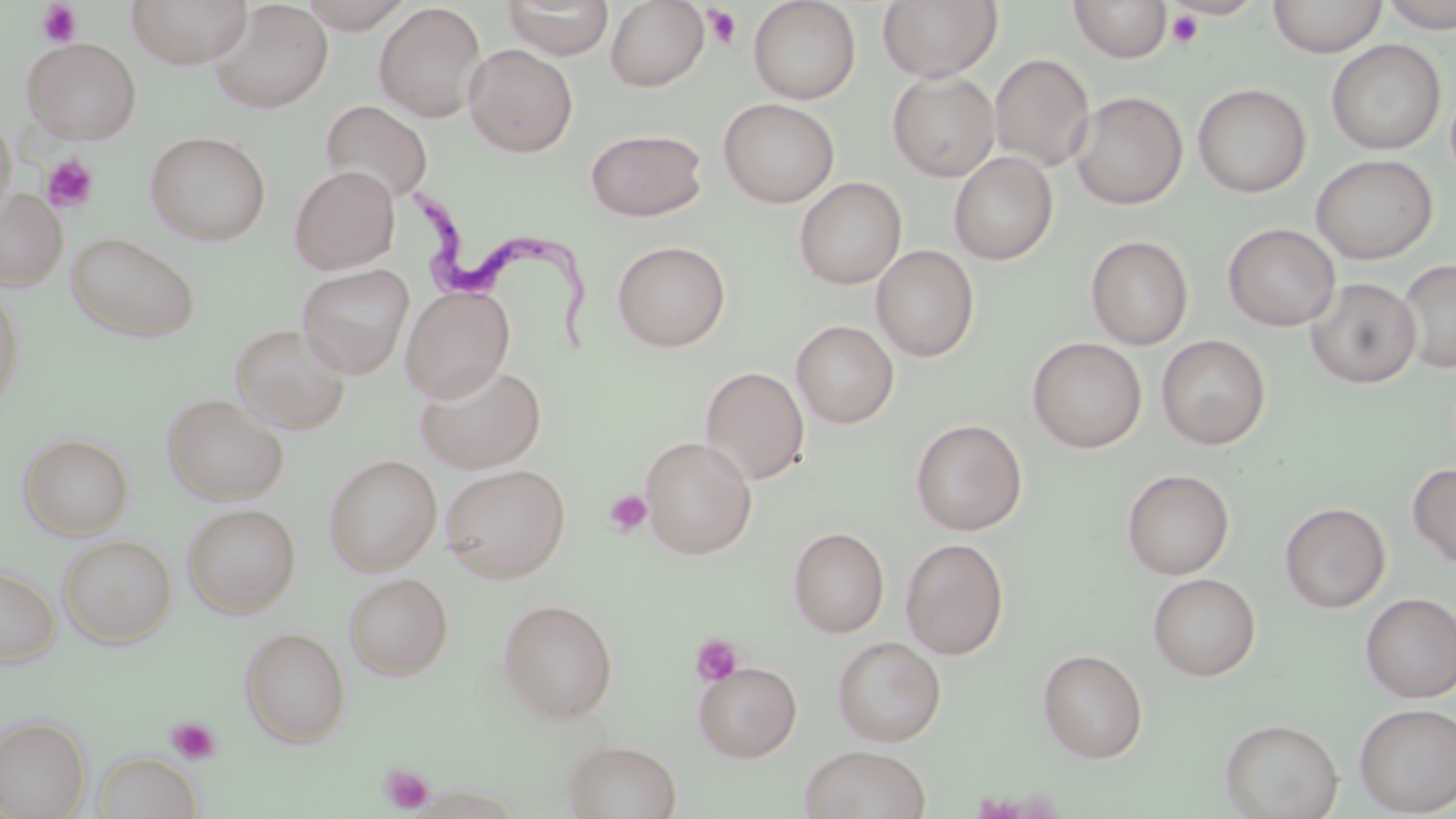
{
  "slide_level_diagnosis": "Trypanosoma brucei",
  "magnification": "1000x",
  "field_of_view": "single",
  "preparation": "thin blood smear",
  "stain": "May-Grünwald-Giemsa",
  "image_size": "1456×819 pixels",
  "modality": "light microscopy",
  "uninfected_red_blood_cell_locations": "approximate bounding boxes as (x1, y1, x2, y2) in pixels: (126, 0, 253, 69), (294, 0, 416, 32), (502, 0, 614, 59), (605, 0, 709, 91), (748, 0, 861, 104), (877, 0, 1003, 83), (1069, 0, 1172, 62), (1268, 0, 1387, 58), (1381, 0, 1455, 34), (208, 1, 332, 115), (374, 3, 487, 122), (21, 37, 142, 144), (1326, 39, 1446, 155), (463, 43, 578, 157), (989, 53, 1095, 171), (887, 70, 1000, 181), (1193, 83, 1311, 198), (1069, 91, 1188, 210), (718, 98, 839, 208), (319, 100, 433, 206), (0, 110, 16, 227), (585, 129, 708, 222), (144, 130, 272, 246), (949, 151, 1058, 265), (1311, 154, 1437, 264), (289, 165, 400, 274), (794, 177, 906, 289), (0, 187, 68, 291), (1222, 223, 1340, 331), (66, 232, 200, 343), (1085, 235, 1194, 349), (612, 240, 731, 351), (871, 244, 980, 362), (1397, 259, 1456, 374), (296, 263, 415, 378), (1306, 277, 1421, 388), (0, 284, 26, 413), (400, 285, 515, 402), (791, 320, 899, 428), (230, 323, 352, 435), (1156, 334, 1271, 449), (1028, 337, 1147, 452), (413, 361, 547, 474), (700, 366, 810, 485), (161, 393, 289, 506), (910, 418, 1028, 535), (18, 433, 134, 540), (640, 437, 757, 560), (323, 453, 442, 575), (440, 463, 571, 583), (1407, 463, 1456, 568), (1121, 468, 1235, 580), (1279, 502, 1391, 613), (181, 503, 301, 618), (788, 527, 889, 637), (57, 534, 177, 648), (900, 537, 1009, 659), (0, 564, 61, 667), (343, 572, 453, 680), (1148, 573, 1261, 681), (1359, 592, 1456, 703), (498, 598, 618, 723), (240, 626, 351, 747), (831, 636, 946, 746), (1037, 648, 1148, 763), (694, 661, 802, 762), (1354, 703, 1456, 816), (0, 714, 91, 818), (1219, 718, 1343, 819), (561, 738, 683, 819), (800, 744, 932, 819), (92, 751, 202, 819)",
  "trypanosoma_brucei_locations": "approximate bounding boxes as (x1, y1, x2, y2) in pixels: (395, 176, 597, 352)",
  "platelet_locations": "approximate bounding boxes as (x1, y1, x2, y2) in pixels: (36, 1, 83, 48), (702, 5, 743, 50), (1166, 10, 1203, 48), (41, 155, 99, 213), (604, 490, 653, 536), (691, 634, 743, 686), (166, 716, 220, 764), (378, 763, 434, 814)"
}